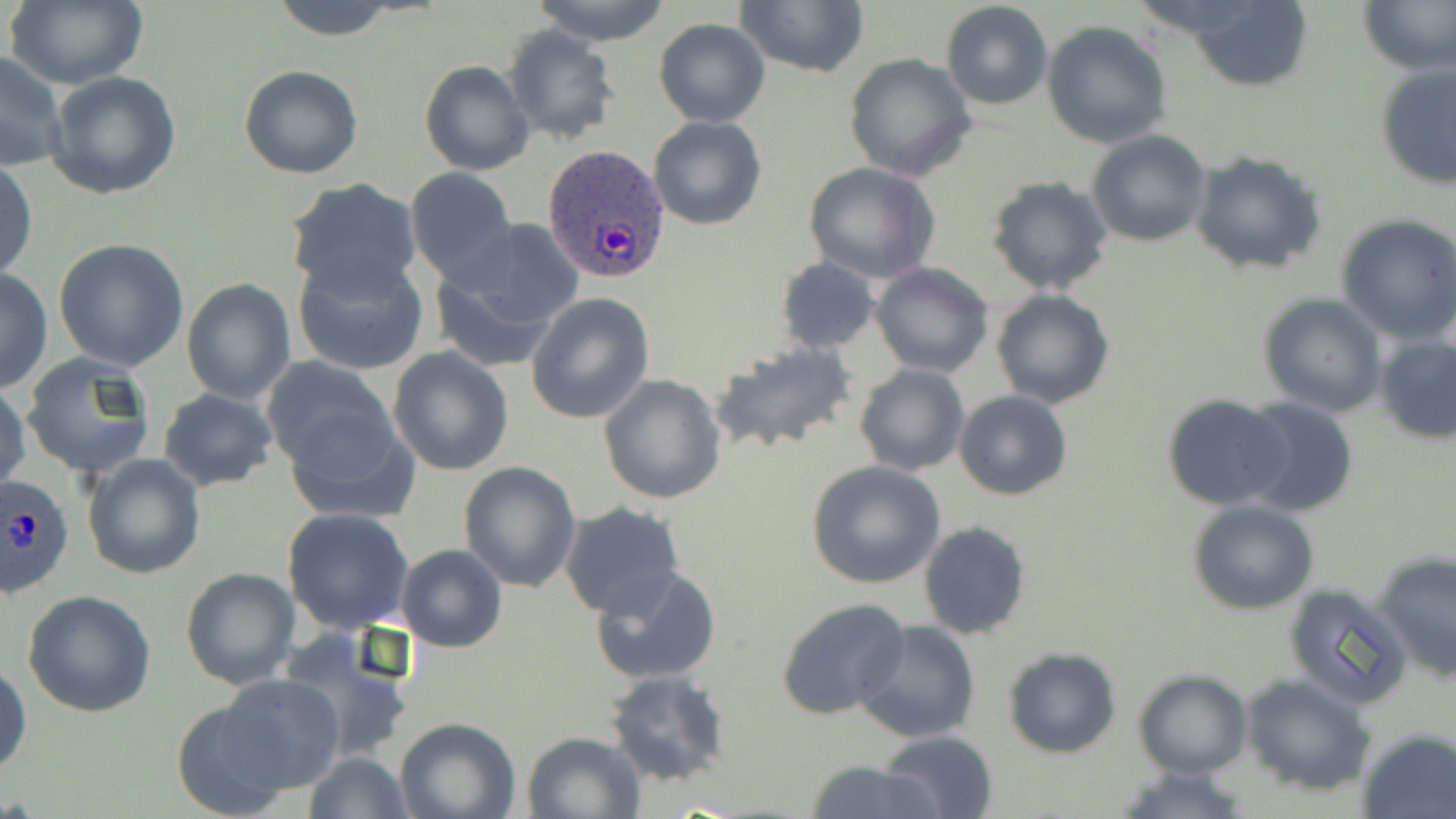

{
  "slide_level_diagnosis": "Plasmodium ovale",
  "field_of_view": "one of a larger specimen",
  "stain": "May-Grünwald-Giemsa",
  "modality": "optical microscopy",
  "plasmodium_ovale_infected_red_blood_cell_locations": "approximate bounding boxes as (x1,y1)-(x2,y2) corner pairs in pixels: (542,144)-(671,285), (0,474)-(76,601)",
  "image_size": "1456×819 pixels",
  "preparation": "thin blood smear",
  "uninfected_red_blood_cell_locations": "approximate bounding boxes as (x1,y1)-(x2,y2) corner pairs in pixels: (6,0)-(150,90), (267,0)-(404,41), (529,0)-(673,45), (734,0)-(870,78), (1356,0)-(1455,75), (941,1)-(1053,110), (1181,2)-(1315,91), (653,18)-(771,127), (1042,20)-(1172,149), (500,25)-(621,145), (1,50)-(69,172), (843,52)-(976,180), (420,60)-(535,177), (1375,64)-(1456,189), (239,65)-(364,180), (47,71)-(182,198), (648,116)-(767,231), (1085,131)-(1212,247), (1189,151)-(1327,277), (0,156)-(37,284), (802,161)-(939,284), (406,167)-(518,287), (985,176)-(1113,296), (285,178)-(421,297), (1335,215)-(1456,342), (429,221)-(584,365), (52,238)-(191,372), (292,251)-(428,376), (775,257)-(879,354), (870,262)-(994,379), (0,267)-(52,394), (182,279)-(295,405), (990,291)-(1114,408), (526,293)-(654,424), (1258,293)-(1386,416), (1374,333)-(1456,445), (710,340)-(858,454), (388,346)-(513,476), (19,352)-(156,479), (263,357)-(405,492), (853,364)-(970,477), (599,375)-(726,504), (0,380)-(31,496), (158,388)-(280,491), (954,390)-(1073,500), (1162,394)-(1294,511), (1237,397)-(1359,516), (280,402)-(419,527), (81,452)-(206,580), (458,460)-(581,593), (805,460)-(947,589), (1187,498)-(1318,614), (558,503)-(688,622), (282,507)-(415,635), (917,521)-(1032,640), (396,544)-(507,653), (1373,551)-(1456,682), (590,564)-(721,686), (180,566)-(300,690), (1282,583)-(1413,709), (24,590)-(157,718), (775,596)-(910,719), (853,620)-(981,742), (280,629)-(416,765), (1003,645)-(1121,758), (0,658)-(32,780), (1134,669)-(1252,778), (604,670)-(732,787), (1239,671)-(1376,796), (201,673)-(348,802), (396,716)-(521,819), (1356,728)-(1456,819), (522,729)-(647,819), (877,730)-(1000,819), (303,751)-(412,819), (801,759)-(947,819), (1110,762)-(1259,819)",
  "magnification": "1000x"
}